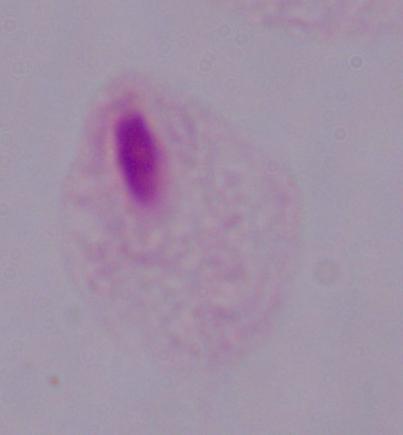
Summary:
  - Identification: trichomonad
  - Modality: micrograph
  - Magnification: 1000x